Assess the morphology of the erythrocytes.
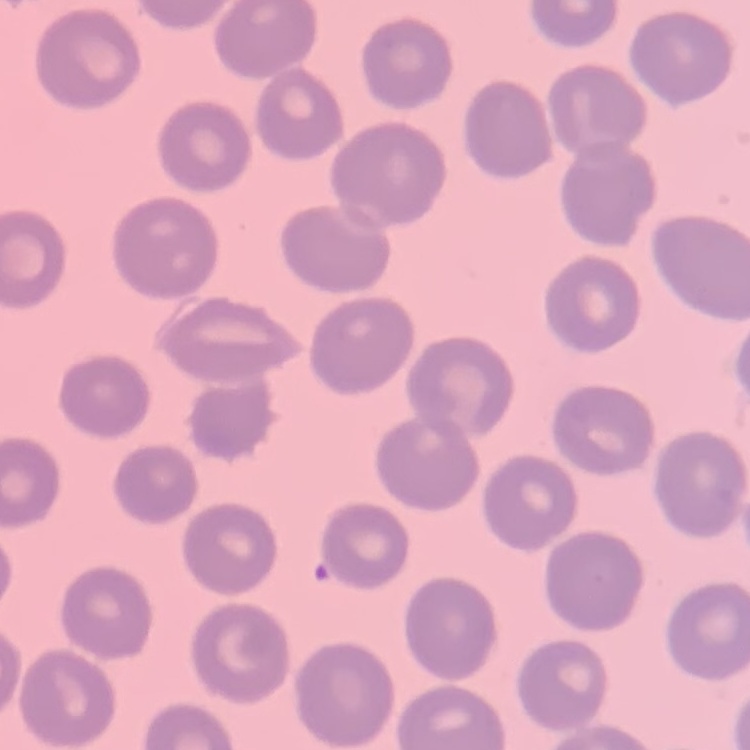

They show no rouleaux formation.

stain: Field's or Giemsa
preparation: thin blood smear
image_type: one tile cut from a larger photomicrograph